Classify this cell by malaria status.
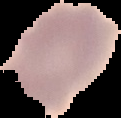
It is uninfected.

Image is 121×118 pixels. Segmented cell region on a black background. From a thin blood film.